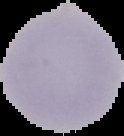
preparation: thin blood film
result: no malaria parasites seen
image_type: segmented cell region with the area outside set to black
image_size: 124×136 pixels